Identify the parasite.
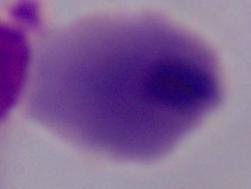

A trichomonad.

Captured at 1000x magnification. Photomicrograph.